Assess this cell for malaria.
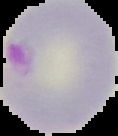

Parasitized.

From a thin blood smear. Cell region segmented out of the field of view; the surrounding area is masked to black. Image is 118×136 pixels.